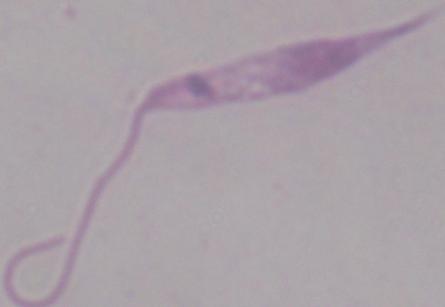
modality = photomicrograph
identification = Leishmania
magnification = 1000x